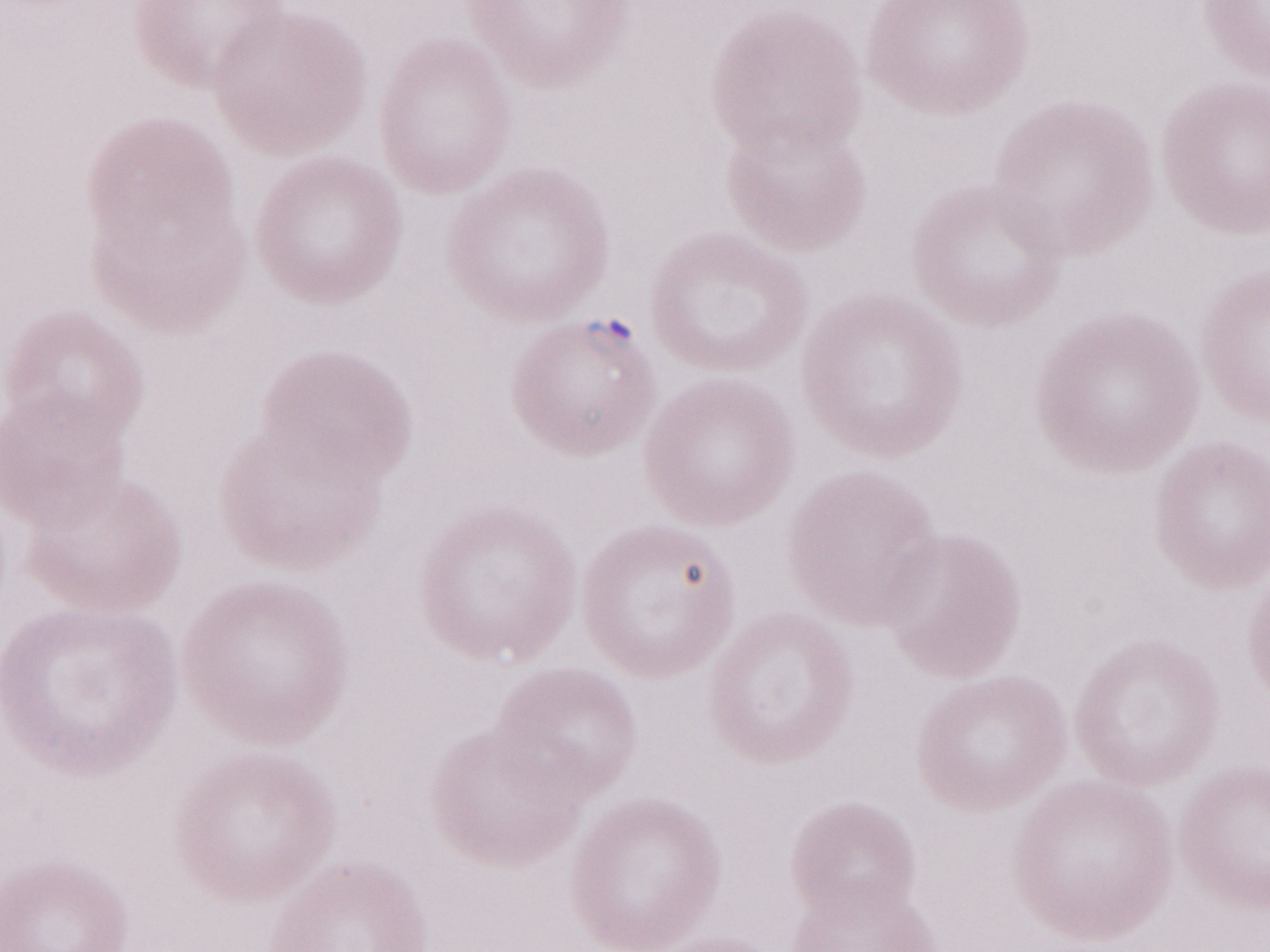
Magnification: 1,000x. One field of this slide. Olympus BX43 microscope, Olympus DP73 camera. Thin blood film. Image is 1270×952 pixels. May-Grünwald-Giemsa stain. Patient-level malaria diagnosis: positive.